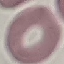
Result: no malaria parasites seen. Thin blood smear. Acquired by smartphone through the microscope eyepiece. Automatically extracted cell patch, resized to 64 × 64 pixels. Giemsa stain.